Comment on the morphology of the red blood cells.
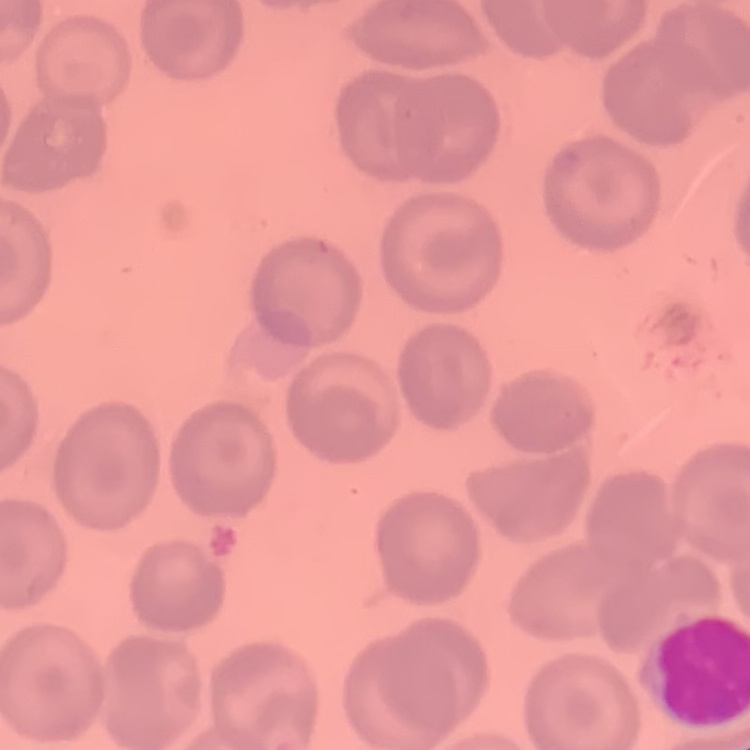

They show no rouleaux formation.

Summary:
  - Preparation: thin peripheral smear
  - Stain: Field's or Giemsa
  - Image type: square crop of a larger photomicrograph